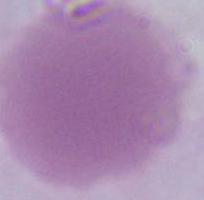

{
  "modality": "photomicrograph",
  "identification": "red blood cell",
  "magnification": "1000x"
}